Report the malaria status of this cell.
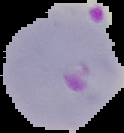
Parasitized.

Summary:
  - Image type: segmented cell region on a black background
  - Preparation: thin blood film
  - Image size: 124×133 pixels